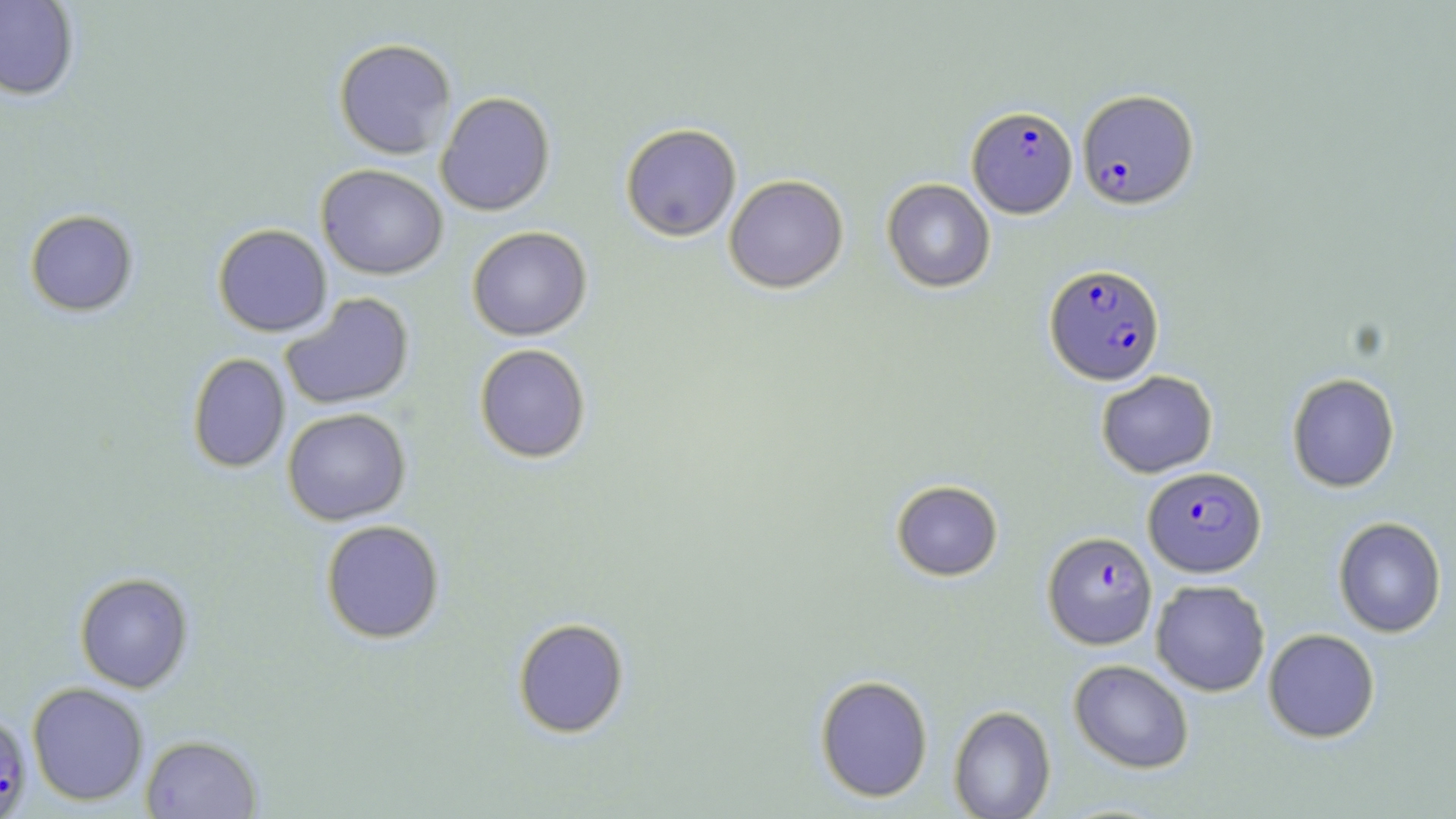
Approximate bounding boxes as named x1/y1/x2/y2 corners in pixels. Plasmodium falciparum-infected red blood cell locations: (x1=1077, y1=89, x2=1198, y2=209), (x1=967, y1=105, x2=1078, y2=218), (x1=1044, y1=263, x2=1166, y2=385), (x1=1143, y1=466, x2=1267, y2=578), (x1=1042, y1=530, x2=1158, y2=650), (x1=0, y1=712, x2=33, y2=816). Uninfected red blood cell locations: (x1=0, y1=0, x2=80, y2=101), (x1=333, y1=38, x2=457, y2=159), (x1=435, y1=91, x2=556, y2=216), (x1=620, y1=123, x2=742, y2=242), (x1=316, y1=164, x2=448, y2=280), (x1=724, y1=174, x2=849, y2=293), (x1=882, y1=178, x2=996, y2=293), (x1=24, y1=209, x2=139, y2=316), (x1=213, y1=224, x2=332, y2=337), (x1=467, y1=226, x2=593, y2=341), (x1=279, y1=293, x2=415, y2=411), (x1=474, y1=344, x2=591, y2=464), (x1=187, y1=353, x2=291, y2=473), (x1=1096, y1=370, x2=1218, y2=478), (x1=1286, y1=372, x2=1400, y2=492), (x1=282, y1=407, x2=411, y2=525), (x1=890, y1=479, x2=1003, y2=581), (x1=1333, y1=516, x2=1447, y2=637), (x1=320, y1=519, x2=445, y2=643), (x1=75, y1=572, x2=193, y2=693), (x1=1150, y1=579, x2=1270, y2=697), (x1=512, y1=617, x2=630, y2=738), (x1=1262, y1=628, x2=1381, y2=743), (x1=1069, y1=659, x2=1194, y2=773), (x1=815, y1=674, x2=933, y2=802), (x1=27, y1=682, x2=149, y2=805), (x1=948, y1=704, x2=1056, y2=819), (x1=141, y1=734, x2=262, y2=818). Slide-level diagnosis: Plasmodium falciparum. Single field of view. Image is 1456×819 pixels. May-Grünwald-Giemsa-stained preparation. Optical microscopy. 1000x magnification. Thin blood film.